Comment on the morphology of the erythrocytes.
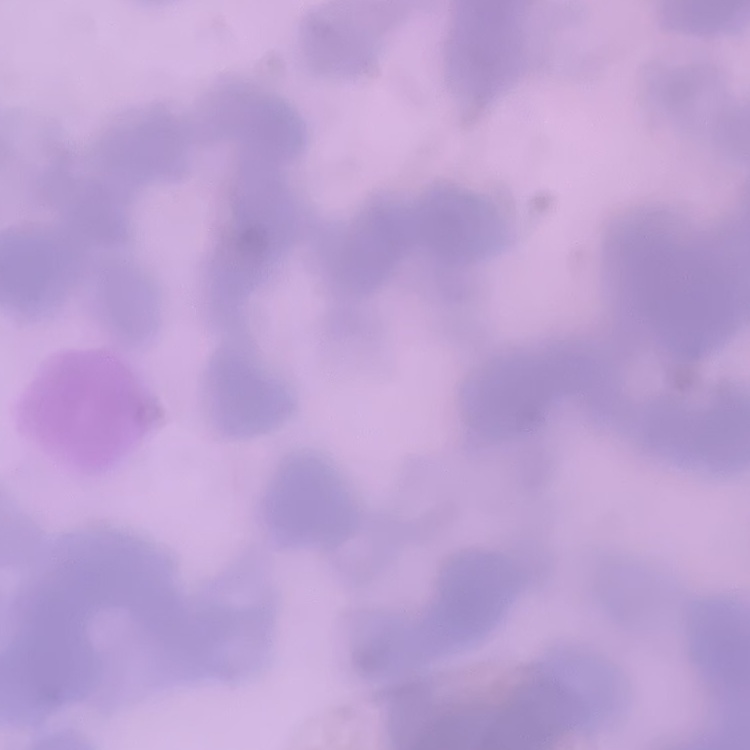
They show rouleaux formation.

Thin blood film. Square crop of a larger photomicrograph. Field's or Giemsa stain.